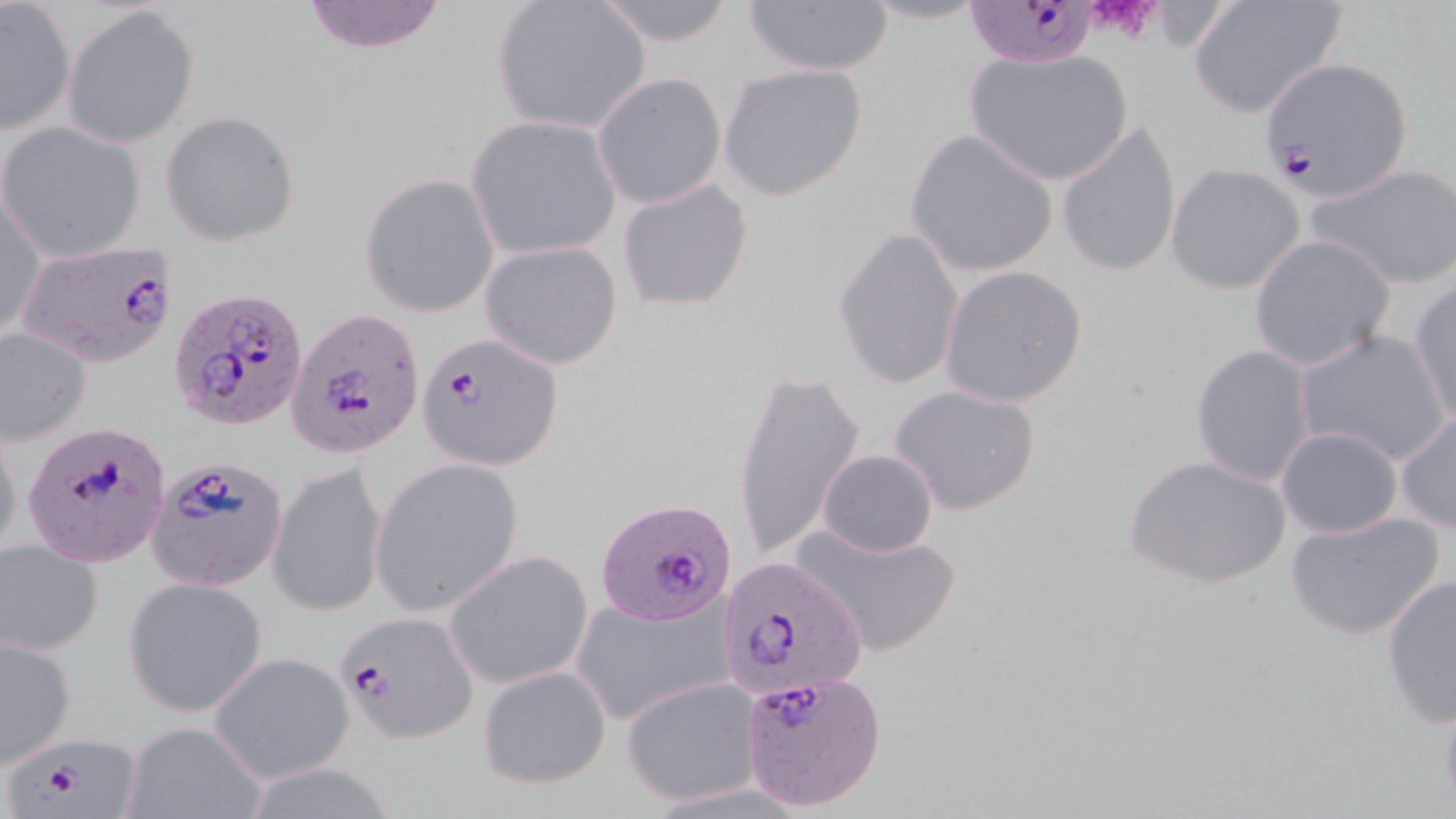 Approximate bounding boxes as named x1/y1/x2/y2 corners in pixels. Plasmodium falciparum-infected red blood cell locations: (x1=976, y1=2, x2=1100, y2=64), (x1=1259, y1=53, x2=1413, y2=198), (x1=19, y1=242, x2=180, y2=368), (x1=171, y1=288, x2=310, y2=431), (x1=288, y1=309, x2=425, y2=458), (x1=418, y1=331, x2=563, y2=469), (x1=22, y1=421, x2=172, y2=570), (x1=147, y1=454, x2=288, y2=591), (x1=597, y1=497, x2=736, y2=626), (x1=720, y1=556, x2=870, y2=706), (x1=335, y1=609, x2=477, y2=742), (x1=741, y1=672, x2=887, y2=812), (x1=7, y1=735, x2=144, y2=815). Platelet locations: (x1=1085, y1=0, x2=1163, y2=43). Uninfected red blood cell locations: (x1=295, y1=0, x2=453, y2=54), (x1=490, y1=0, x2=652, y2=135), (x1=857, y1=0, x2=994, y2=26), (x1=594, y1=1, x2=739, y2=47), (x1=743, y1=1, x2=893, y2=77), (x1=1, y1=2, x2=76, y2=133), (x1=1188, y1=2, x2=1348, y2=118), (x1=65, y1=4, x2=198, y2=147), (x1=963, y1=47, x2=1133, y2=186), (x1=719, y1=63, x2=867, y2=201), (x1=593, y1=72, x2=726, y2=210), (x1=160, y1=108, x2=302, y2=246), (x1=466, y1=115, x2=621, y2=259), (x1=1056, y1=120, x2=1182, y2=278), (x1=1, y1=122, x2=148, y2=262), (x1=905, y1=128, x2=1060, y2=280), (x1=1309, y1=162, x2=1456, y2=289), (x1=1166, y1=164, x2=1305, y2=293), (x1=359, y1=172, x2=499, y2=317), (x1=617, y1=177, x2=754, y2=314), (x1=1, y1=188, x2=45, y2=345), (x1=832, y1=226, x2=967, y2=392), (x1=1248, y1=235, x2=1395, y2=371), (x1=480, y1=240, x2=624, y2=370), (x1=939, y1=264, x2=1089, y2=408), (x1=1410, y1=280, x2=1456, y2=428), (x1=1295, y1=327, x2=1452, y2=468), (x1=0, y1=328, x2=94, y2=446), (x1=1191, y1=344, x2=1316, y2=486), (x1=730, y1=368, x2=864, y2=560), (x1=888, y1=384, x2=1043, y2=516), (x1=1396, y1=410, x2=1456, y2=533), (x1=0, y1=417, x2=22, y2=568), (x1=1275, y1=426, x2=1403, y2=539), (x1=818, y1=449, x2=937, y2=558), (x1=1126, y1=453, x2=1291, y2=592), (x1=369, y1=459, x2=523, y2=617), (x1=268, y1=460, x2=388, y2=618), (x1=1284, y1=510, x2=1447, y2=642), (x1=794, y1=519, x2=960, y2=659), (x1=0, y1=538, x2=103, y2=655), (x1=444, y1=548, x2=594, y2=690), (x1=1380, y1=575, x2=1456, y2=726), (x1=123, y1=578, x2=267, y2=716), (x1=571, y1=588, x2=737, y2=727), (x1=0, y1=634, x2=77, y2=768), (x1=210, y1=652, x2=353, y2=783), (x1=478, y1=663, x2=612, y2=791), (x1=623, y1=677, x2=762, y2=805), (x1=1437, y1=684, x2=1456, y2=817), (x1=121, y1=721, x2=268, y2=817). Slide-level diagnosis: Plasmodium falciparum. May-Grünwald-Giemsa stain. Captured at 1000x magnification. Image is 1456×819 pixels. Single field of view. Thin blood film. Light microscopy.